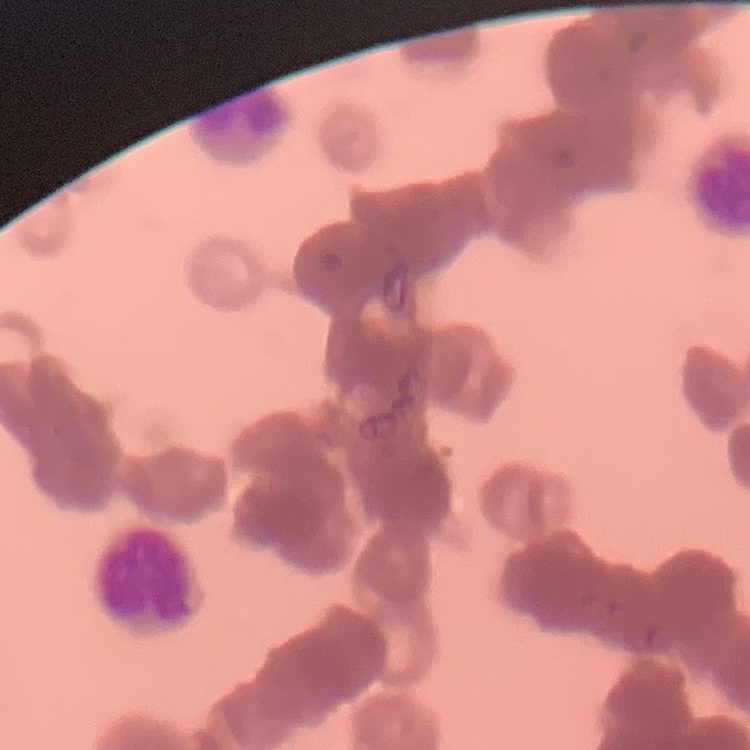
{
  "erythrocyte_morphology": "rouleaux formation",
  "stain": "Field's or Giemsa",
  "preparation": "thin blood smear",
  "image_type": "square crop of a larger photomicrograph"
}